Outline each Plasmodium malariae-infected red blood cell.
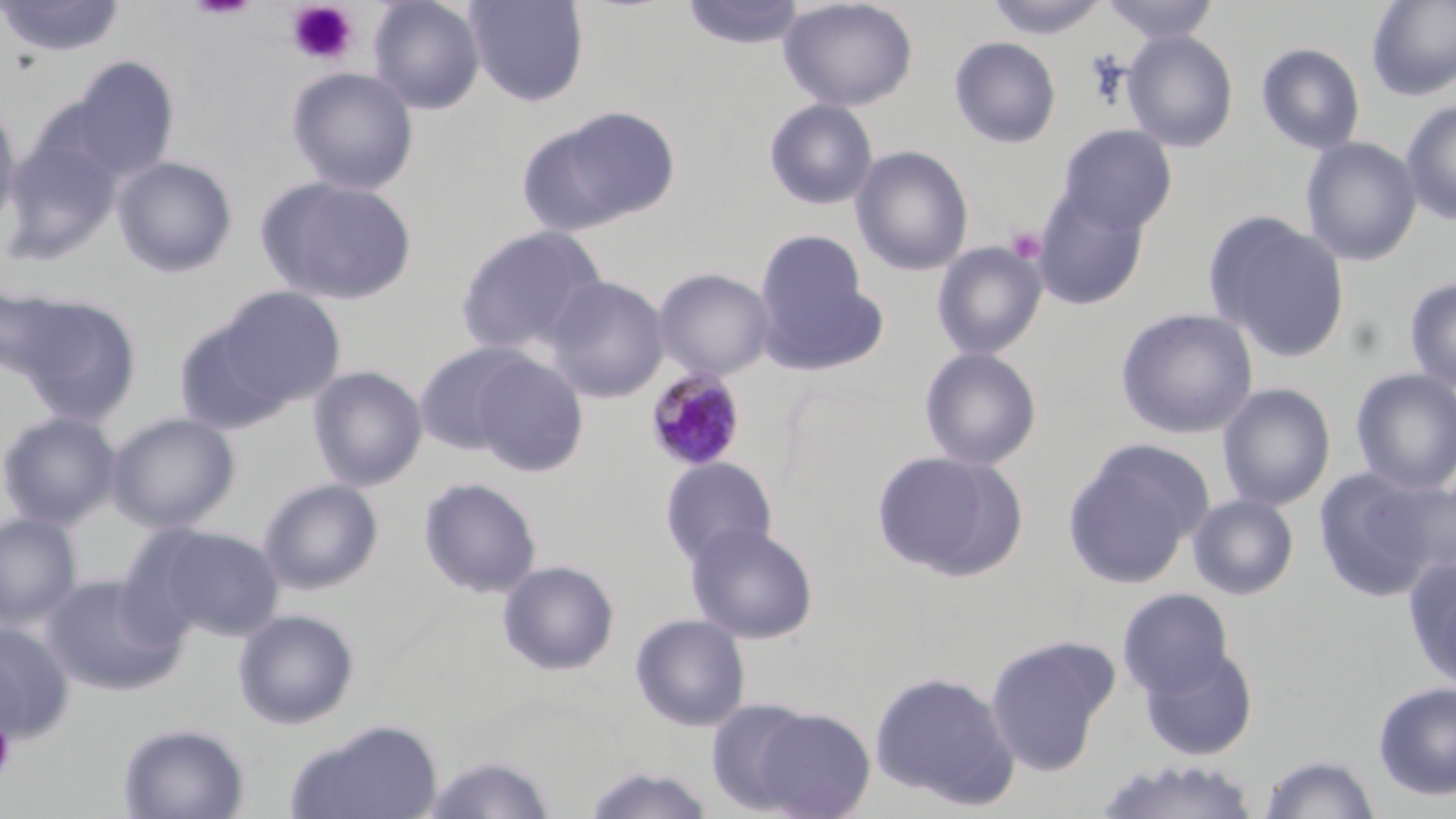
Approximate bounding boxes as (x1,y1)-(x2,y2) corner pairs in pixels.
Plasmodium malariae-infected red blood cells: (645,366)-(746,472).

Summary:
  - Uninfected red blood cell locations: (0,0)-(125,59), (367,0)-(486,114), (464,0)-(590,106), (680,0)-(806,50), (777,0)-(919,111), (1100,0)-(1221,43), (1365,0)-(1456,102), (982,1)-(1112,39), (1122,30)-(1239,152), (949,36)-(1061,148), (1256,42)-(1365,154), (67,57)-(179,182), (286,66)-(420,195), (764,98)-(879,210), (1400,98)-(1456,225), (0,101)-(22,237), (545,106)-(684,225), (1057,124)-(1178,234), (1,131)-(122,262), (1300,136)-(1422,266), (851,145)-(974,276), (113,155)-(238,278), (257,175)-(418,306), (1032,186)-(1150,310), (1205,211)-(1350,361), (455,224)-(607,356), (755,229)-(872,342), (931,241)-(1048,360), (759,266)-(889,377), (653,267)-(776,380), (546,276)-(669,402), (1403,277)-(1456,392), (0,283)-(74,382), (211,286)-(347,410), (11,293)-(142,426), (1115,306)-(1259,439), (171,314)-(300,435), (413,342)-(537,455), (919,347)-(1042,470), (471,354)-(588,477), (308,365)-(428,491), (1350,368)-(1456,494), (1217,382)-(1336,511), (0,410)-(122,529), (106,412)-(240,533), (1062,440)-(1211,589), (872,449)-(1028,582), (659,456)-(777,568), (1313,467)-(1446,602), (418,477)-(542,599), (258,478)-(384,595), (1188,493)-(1299,600), (0,513)-(81,628), (685,522)-(819,645), (136,524)-(284,642), (1405,556)-(1456,694), (497,560)-(620,675), (42,574)-(184,696), (1117,587)-(1236,700), (233,609)-(360,729), (630,613)-(751,731), (0,623)-(74,742), (984,633)-(1119,774), (1137,643)-(1259,760), (869,669)-(1021,810), (1373,681)-(1456,800), (706,698)-(819,815), (747,705)-(877,818), (285,718)-(443,819), (117,722)-(250,819), (421,753)-(558,819), (1258,753)-(1381,819), (1091,756)-(1262,819), (581,766)-(717,818)
  - Platelet locations: (285,2)-(359,66), (1006,227)-(1046,263), (0,722)-(16,778)
  - Slide-level diagnosis: Plasmodium malariae
  - Modality: optical microscopy
  - Magnification: 1000x
  - Stain: May-Grünwald-Giemsa
  - Image size: 1456×819 pixels
  - Field of view: single
  - Preparation: thin blood film